Classify this cell by malaria status.
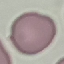
Uninfected.

{
  "stain": "Giemsa",
  "image_type": "automatically extracted cell patch, resized to 64 × 64 pixels",
  "preparation": "thin blood smear",
  "capture": "smartphone through the microscope eyepiece"
}